Classify this cell by malaria status.
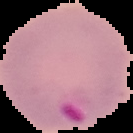
Parasitized.

Image is 133×133 pixels. From a thin blood smear. The area outside the segmented cell region is set to black.